Outline each Plasmodium vivax-infected red blood cell.
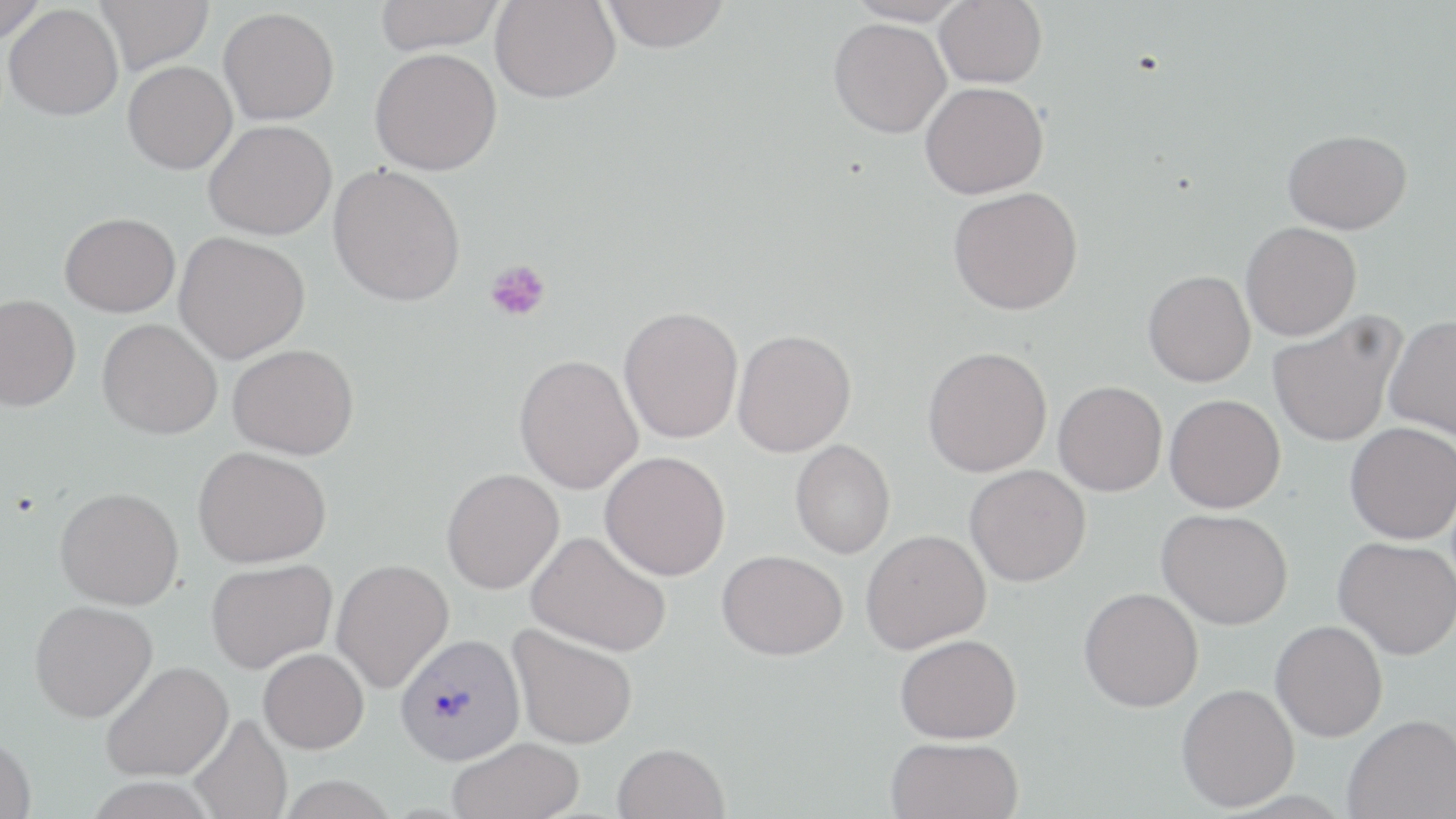
Approximate bounding boxes as (x1, y1, x2, y2) in pixels.
Plasmodium vivax-infected red blood cells: (395, 633, 525, 765).

Summary:
  - Platelet locations: (485, 258, 551, 323)
  - Uninfected red blood cell locations: (0, 0, 47, 45), (94, 0, 213, 75), (374, 0, 505, 53), (601, 0, 731, 52), (846, 0, 969, 27), (935, 0, 1047, 88), (490, 1, 620, 103), (3, 4, 123, 120), (219, 7, 339, 125), (828, 17, 951, 138), (370, 47, 502, 175), (122, 61, 237, 174), (920, 81, 1048, 199), (204, 120, 336, 240), (1283, 129, 1412, 234), (328, 163, 465, 306), (947, 187, 1083, 315), (59, 212, 180, 317), (1241, 221, 1362, 341), (174, 232, 311, 363), (1143, 270, 1256, 387), (0, 294, 81, 412), (618, 305, 743, 443), (1268, 313, 1405, 447), (1383, 315, 1456, 441), (98, 318, 222, 440), (732, 329, 856, 457), (228, 343, 359, 460), (922, 346, 1053, 477), (514, 354, 643, 494), (1054, 380, 1167, 496), (1164, 394, 1286, 513), (1345, 422, 1456, 544), (790, 439, 895, 559), (194, 446, 331, 568), (600, 451, 730, 580), (964, 464, 1091, 587), (442, 468, 564, 594), (55, 487, 184, 610), (1157, 508, 1293, 629), (861, 529, 991, 654), (526, 530, 671, 657), (1334, 536, 1456, 659), (717, 549, 848, 660), (206, 558, 337, 673), (331, 559, 454, 692), (1079, 587, 1204, 712), (30, 600, 158, 722), (1270, 620, 1388, 742), (508, 623, 638, 749), (895, 634, 1022, 744), (259, 648, 369, 753), (101, 661, 233, 782), (1176, 683, 1299, 811), (189, 714, 292, 819), (1343, 714, 1456, 819), (0, 733, 36, 819), (885, 736, 1023, 819), (447, 737, 585, 819), (612, 743, 729, 819)
  - Slide-level diagnosis: Plasmodium vivax
  - Preparation: thin blood smear
  - Magnification: 1000x
  - Modality: optical microscopy
  - Field of view: one of a larger specimen
  - Image size: 1456×819 pixels
  - Stain: May-Grünwald-Giemsa